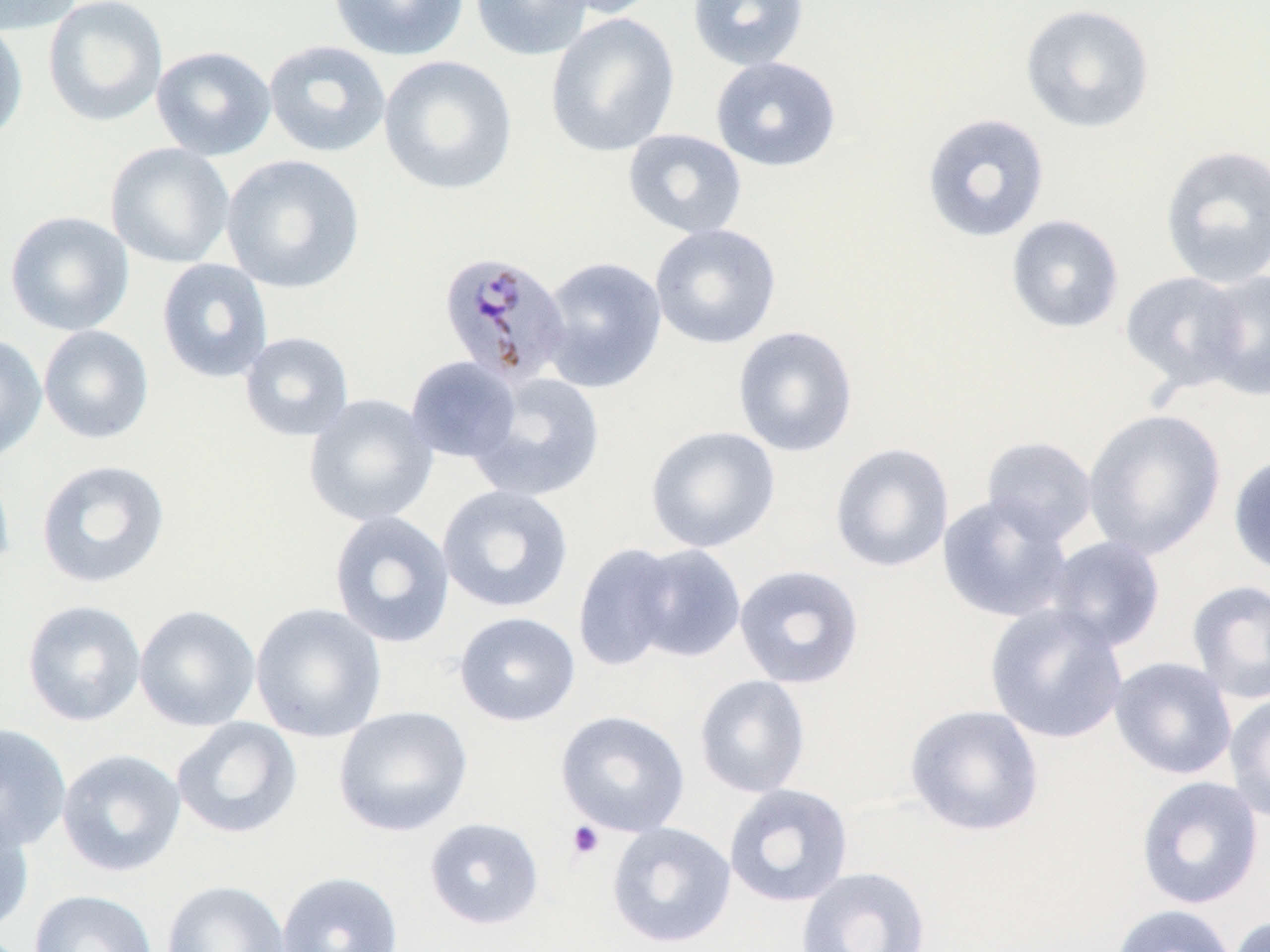

Approximate bounding boxes as (x1, y1, x2, y2) in pixels. Platelet locations: (566, 820, 604, 861). Uninfected red blood cell locations: (0, 0, 82, 35), (43, 0, 169, 127), (328, 0, 469, 61), (469, 0, 595, 61), (546, 0, 666, 20), (687, 0, 810, 71), (1019, 3, 1155, 135), (545, 13, 680, 157), (0, 18, 29, 145), (263, 39, 391, 158), (151, 45, 277, 160), (378, 55, 518, 196), (710, 56, 842, 173), (921, 112, 1051, 243), (623, 128, 748, 239), (105, 142, 236, 269), (1159, 144, 1270, 289), (221, 154, 365, 294), (4, 210, 135, 336), (1005, 214, 1125, 334), (649, 223, 782, 349), (537, 255, 668, 393), (156, 258, 274, 384), (1196, 269, 1270, 402), (1119, 270, 1250, 392), (38, 325, 154, 444), (732, 325, 859, 458), (239, 331, 355, 442), (0, 333, 47, 465), (404, 356, 521, 463), (469, 372, 605, 503), (303, 393, 439, 527), (1082, 409, 1226, 560), (644, 424, 781, 554), (980, 436, 1098, 546), (829, 442, 955, 573), (1228, 452, 1270, 579), (0, 453, 15, 583), (35, 459, 171, 589), (437, 484, 575, 614), (937, 493, 1075, 623), (328, 510, 456, 648), (1042, 535, 1166, 653), (571, 542, 683, 672), (627, 543, 747, 662), (733, 564, 865, 689), (1186, 580, 1270, 704), (21, 599, 146, 727), (250, 602, 387, 743), (984, 603, 1129, 744), (134, 604, 261, 731), (454, 611, 580, 726), (1109, 656, 1237, 780), (694, 674, 812, 798), (1223, 692, 1270, 823), (904, 704, 1045, 837), (333, 705, 473, 837), (555, 710, 690, 837), (171, 716, 303, 840), (0, 723, 72, 852), (57, 748, 186, 877), (1135, 775, 1265, 910), (723, 783, 854, 908), (0, 806, 35, 936), (424, 817, 544, 930), (605, 821, 736, 948), (796, 865, 932, 952), (276, 871, 404, 952), (161, 879, 290, 952), (29, 889, 159, 952), (1110, 904, 1240, 952), (1227, 915, 1269, 952). Plasmodium malariae-infected red blood cell locations: (437, 251, 571, 387). Slide-level diagnosis: Plasmodium malariae. 1000x magnification. Image is 1270×952 pixels. Thin blood smear. One field of a larger specimen. Light microscopy. May-Grünwald-Giemsa stain.